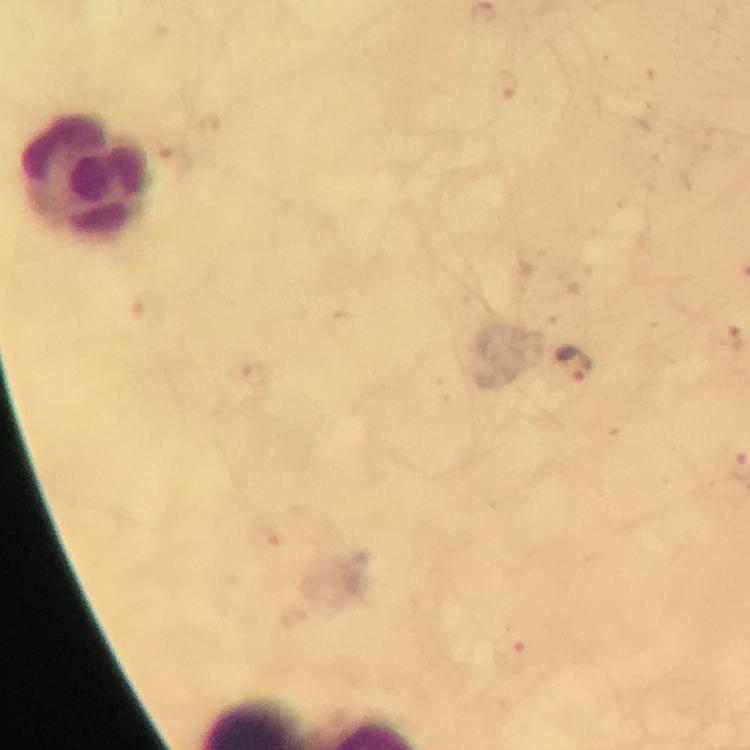

Approximate object centers, in pixels from the top-left corner. Malaria parasite locations: (x=507, y=85), (x=175, y=162), (x=729, y=337), (x=573, y=363), (x=268, y=539), (x=512, y=656). Leukocyte locations: (x=86, y=176). Photographed with a smartphone mounted on the microscope. Immersion oil was used. Image is 750×750 pixels. Giemsa-stained preparation. From a diagnostic examination for malaria. Thick smear. 100x magnification. A crop from one field of view.